State the preparation type.
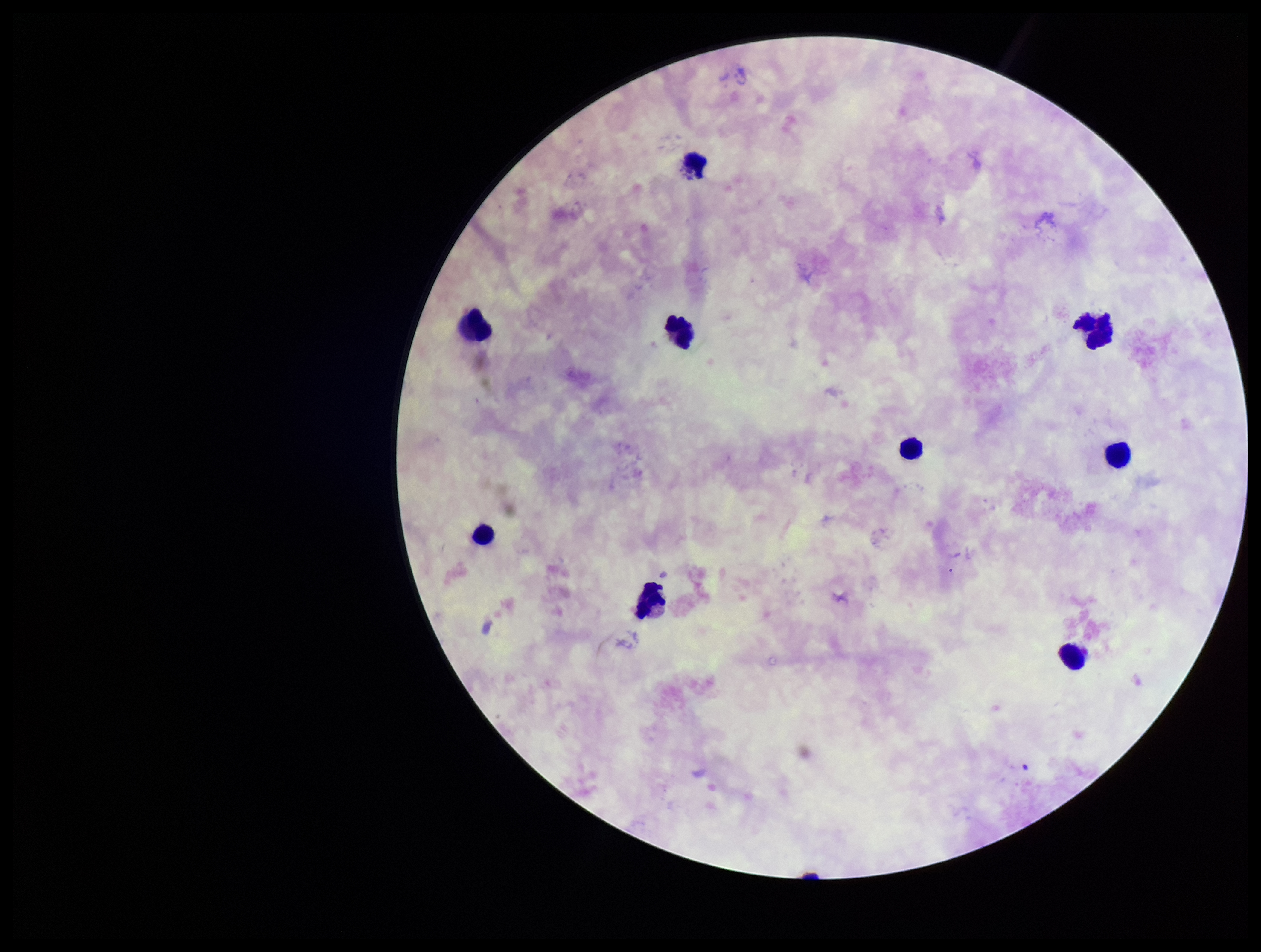
It is a thick blood smear.

{
  "leukocyte_count": 9,
  "plasmodium_parasites": "none detected",
  "parasite_count": 0,
  "field_of_view": "one from this slide",
  "stain": "Giemsa",
  "patient_malaria_status": "negative",
  "image_size": "1261×952 pixels",
  "capture": "smartphone photograph through the microscope eyepiece"
}